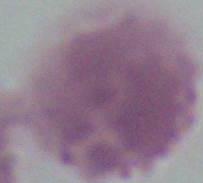

{
  "identification": "erythrocyte",
  "modality": "micrograph",
  "magnification": "1000x"
}